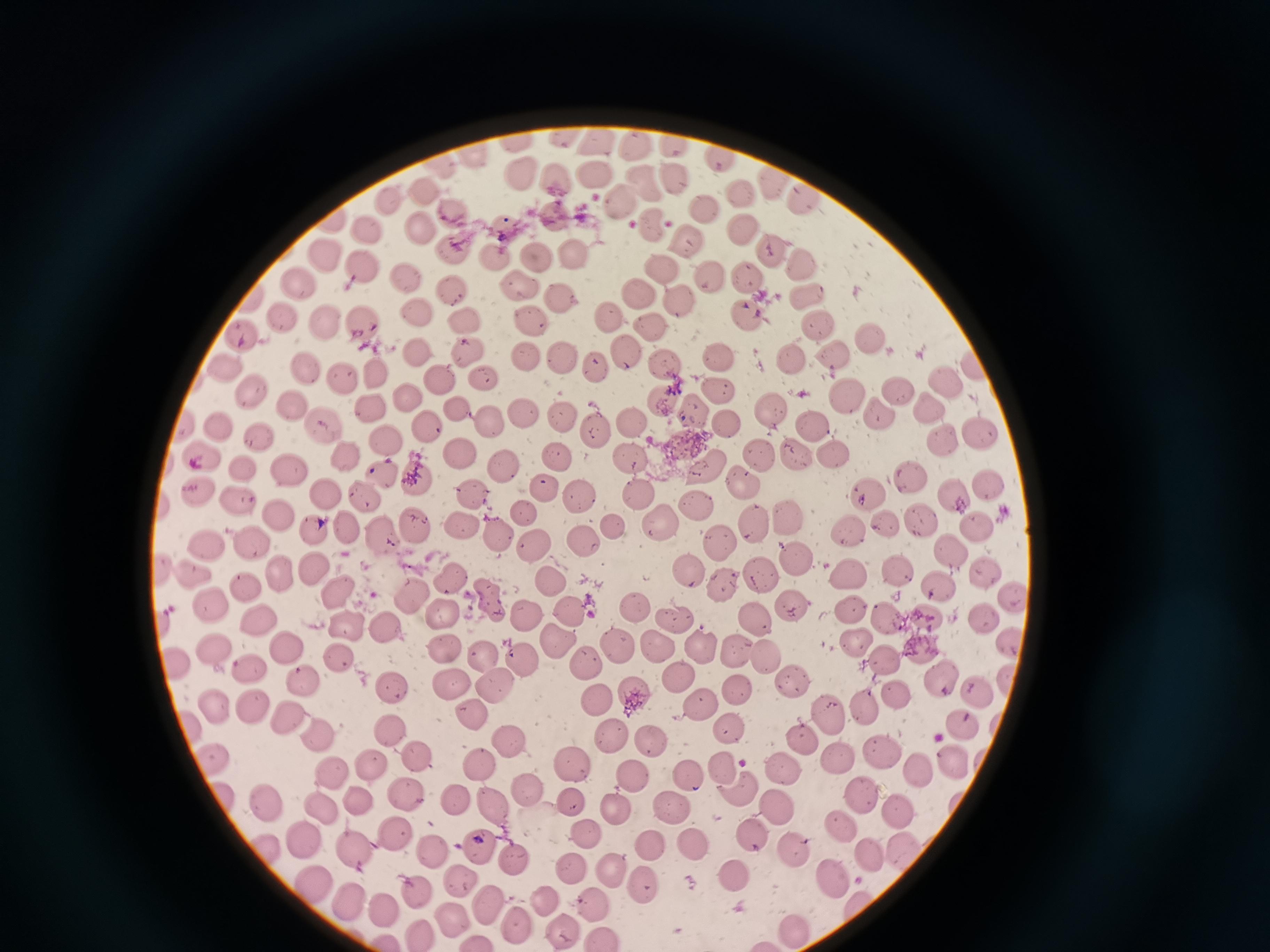

cell locations = approximate object centers, in pixels from the top-left corner: (x=600, y=141), (x=631, y=145), (x=670, y=147), (x=472, y=156), (x=713, y=158), (x=591, y=174), (x=520, y=177), (x=671, y=179), (x=556, y=180), (x=765, y=183), (x=645, y=189), (x=737, y=190), (x=424, y=194), (x=390, y=198), (x=799, y=199), (x=616, y=201), (x=702, y=208), (x=456, y=215), (x=551, y=221), (x=504, y=227), (x=413, y=229), (x=654, y=230), (x=747, y=230), (x=369, y=232), (x=688, y=239), (x=454, y=249), (x=769, y=252), (x=576, y=254), (x=494, y=256), (x=322, y=258), (x=807, y=260), (x=536, y=261), (x=367, y=267), (x=665, y=267), (x=711, y=273), (x=748, y=277), (x=404, y=278), (x=300, y=285), (x=517, y=286), (x=452, y=290), (x=638, y=292), (x=808, y=294), (x=565, y=299), (x=683, y=303), (x=416, y=312), (x=461, y=313), (x=747, y=315), (x=283, y=316), (x=609, y=316), (x=533, y=320), (x=653, y=321), (x=814, y=324), (x=329, y=326), (x=363, y=327), (x=869, y=333), (x=248, y=339), (x=465, y=350), (x=626, y=350), (x=835, y=351), (x=418, y=352), (x=721, y=353), (x=560, y=354), (x=791, y=355), (x=528, y=358), (x=599, y=363), (x=664, y=363), (x=308, y=369), (x=229, y=372), (x=378, y=374), (x=342, y=377), (x=439, y=377), (x=485, y=381), (x=943, y=383), (x=717, y=389), (x=896, y=390), (x=252, y=394), (x=408, y=394), (x=846, y=396), (x=662, y=400), (x=295, y=404), (x=454, y=405), (x=766, y=407), (x=928, y=407), (x=373, y=408), (x=692, y=410), (x=525, y=411), (x=560, y=412), (x=875, y=413), (x=628, y=420), (x=727, y=420), (x=809, y=420), (x=222, y=422), (x=329, y=422), (x=486, y=423), (x=427, y=426), (x=592, y=429), (x=260, y=434), (x=977, y=434), (x=941, y=439), (x=387, y=443), (x=830, y=451), (x=457, y=452), (x=799, y=453), (x=555, y=454), (x=629, y=454), (x=761, y=456), (x=203, y=461), (x=343, y=461), (x=248, y=464), (x=704, y=465), (x=381, y=468), (x=287, y=470), (x=419, y=475), (x=916, y=478), (x=985, y=483), (x=743, y=484), (x=541, y=486), (x=642, y=490), (x=578, y=492), (x=203, y=493), (x=319, y=493), (x=865, y=493), (x=952, y=493), (x=471, y=496), (x=365, y=497), (x=241, y=499), (x=696, y=507), (x=523, y=513), (x=274, y=514), (x=788, y=518), (x=919, y=520), (x=661, y=521), (x=459, y=522), (x=757, y=523), (x=975, y=523), (x=615, y=526), (x=886, y=526), (x=411, y=527), (x=346, y=529), (x=375, y=533), (x=497, y=533), (x=313, y=534), (x=849, y=537), (x=724, y=539), (x=586, y=540), (x=208, y=541), (x=254, y=544), (x=533, y=547), (x=951, y=555), (x=796, y=557), (x=311, y=567), (x=984, y=567), (x=686, y=568), (x=896, y=568), (x=280, y=574), (x=759, y=574), (x=851, y=574), (x=194, y=575), (x=452, y=575), (x=553, y=578), (x=720, y=582), (x=935, y=586), (x=246, y=587), (x=407, y=590), (x=336, y=594), (x=1014, y=595), (x=490, y=601), (x=210, y=605), (x=851, y=607), (x=443, y=608), (x=638, y=608), (x=791, y=608), (x=575, y=611), (x=888, y=616), (x=676, y=617), (x=982, y=617), (x=256, y=618), (x=525, y=618), (x=925, y=618), (x=757, y=622), (x=377, y=624), (x=344, y=626), (x=1011, y=634), (x=854, y=641), (x=553, y=643), (x=656, y=643), (x=445, y=645), (x=284, y=647), (x=621, y=647), (x=700, y=649), (x=736, y=650), (x=922, y=650), (x=214, y=652), (x=339, y=656), (x=485, y=656), (x=884, y=658), (x=522, y=659), (x=774, y=660), (x=174, y=661), (x=583, y=662), (x=246, y=667), (x=941, y=674), (x=678, y=675), (x=302, y=680), (x=793, y=681), (x=455, y=685), (x=495, y=687), (x=389, y=688), (x=980, y=688), (x=631, y=690), (x=737, y=691), (x=899, y=696), (x=598, y=699), (x=208, y=703), (x=253, y=704), (x=701, y=706), (x=864, y=707), (x=469, y=714), (x=831, y=714), (x=288, y=716), (x=964, y=720), (x=186, y=726), (x=315, y=732), (x=391, y=732), (x=728, y=733), (x=650, y=738), (x=608, y=739), (x=801, y=740), (x=507, y=743), (x=880, y=750), (x=422, y=754), (x=836, y=755), (x=209, y=757), (x=958, y=761), (x=371, y=762), (x=479, y=762), (x=572, y=763), (x=724, y=768), (x=781, y=768), (x=332, y=771), (x=923, y=771), (x=633, y=774), (x=690, y=779), (x=739, y=788), (x=865, y=790), (x=524, y=791), (x=406, y=792), (x=355, y=797), (x=449, y=798), (x=568, y=799), (x=264, y=800), (x=495, y=805), (x=612, y=805), (x=773, y=805), (x=318, y=806), (x=675, y=809), (x=898, y=811), (x=845, y=821), (x=398, y=831), (x=751, y=834), (x=305, y=836), (x=586, y=836), (x=651, y=843), (x=479, y=845), (x=693, y=846), (x=793, y=849), (x=904, y=851), (x=264, y=852), (x=356, y=853), (x=866, y=854), (x=428, y=855), (x=516, y=858), (x=607, y=864), (x=571, y=865), (x=734, y=875), (x=833, y=875), (x=643, y=879), (x=311, y=881), (x=461, y=882), (x=414, y=892), (x=340, y=893), (x=546, y=897), (x=484, y=899), (x=379, y=904), (x=591, y=906), (x=451, y=913), (x=516, y=922), (x=796, y=928), (x=564, y=931), (x=419, y=933), (x=386, y=939)
field of view = single
preparation = thin blood film
image size = 1270×952 pixels
capture = smartphone through the microscope eyepiece
stain = Giemsa